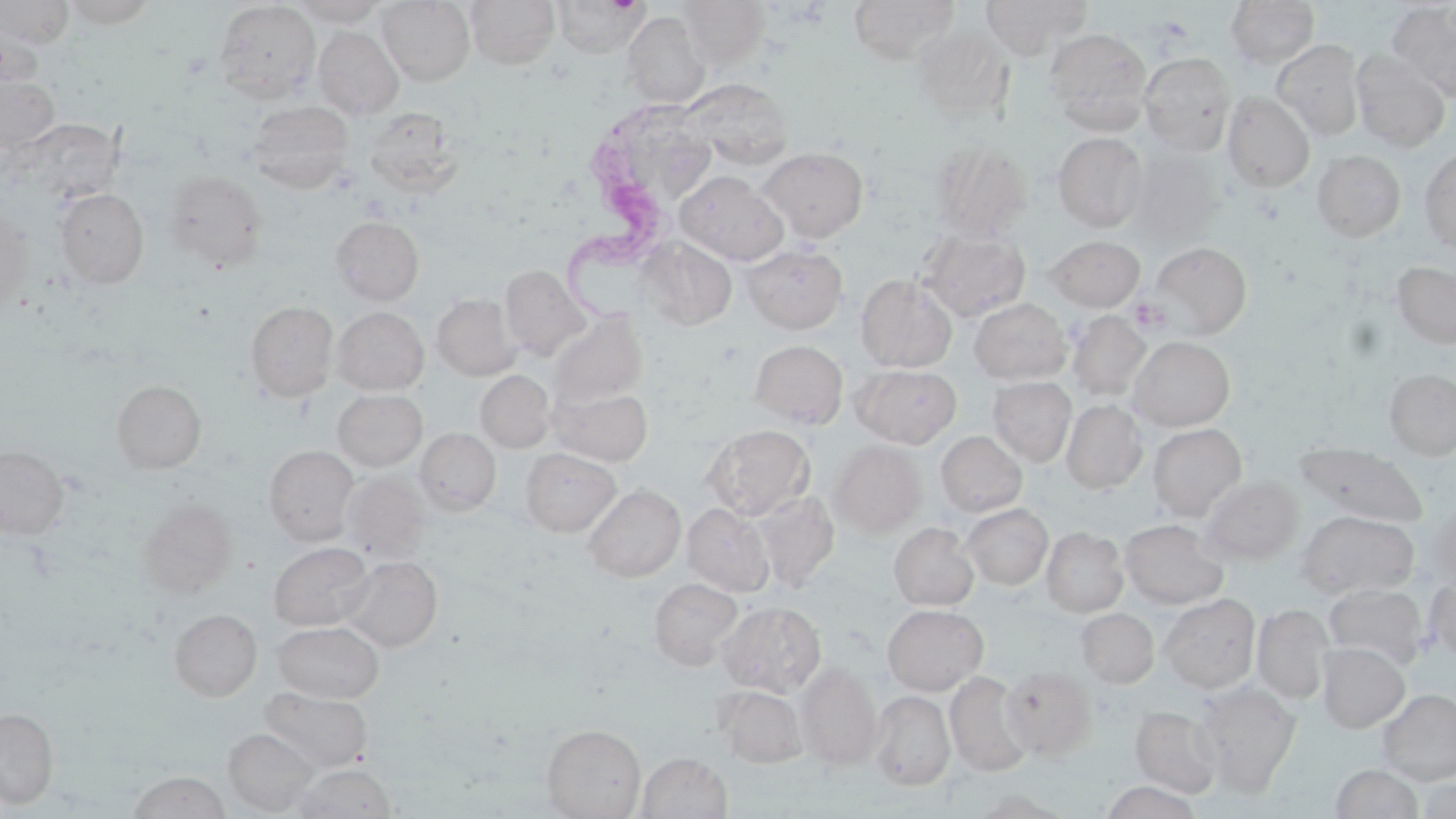
Approximate bounding boxes as [x1, y1, x2, y2] in pixels. Trypanosoma brucei locations: [567, 107, 682, 325]. Uninfected red blood cell locations: [59, 0, 161, 28], [290, 0, 391, 27], [377, 0, 475, 86], [465, 0, 560, 70], [553, 0, 649, 59], [849, 0, 960, 65], [979, 0, 1092, 59], [1225, 0, 1320, 69], [0, 1, 74, 47], [677, 1, 770, 68], [213, 2, 320, 102], [1387, 2, 1456, 102], [622, 11, 710, 109], [0, 19, 45, 94], [911, 24, 1015, 125], [313, 26, 404, 120], [1044, 27, 1153, 135], [1271, 39, 1365, 141], [1350, 50, 1451, 152], [1139, 52, 1237, 155], [0, 75, 61, 156], [681, 78, 793, 169], [1222, 92, 1315, 192], [246, 100, 354, 193], [364, 106, 461, 195], [642, 112, 713, 208], [5, 118, 127, 214], [1053, 132, 1148, 231], [929, 141, 1033, 241], [757, 147, 869, 243], [1126, 147, 1224, 244], [1419, 148, 1456, 254], [1312, 150, 1406, 242], [162, 170, 267, 272], [675, 170, 787, 265], [54, 188, 149, 289], [0, 206, 35, 315], [330, 215, 424, 305], [918, 229, 1030, 321], [1045, 235, 1145, 311], [637, 237, 737, 330], [1149, 241, 1252, 338], [743, 243, 848, 333], [1391, 260, 1456, 349], [499, 264, 590, 360], [855, 274, 958, 372], [432, 292, 520, 380], [969, 298, 1071, 384], [244, 300, 339, 402], [332, 307, 429, 395], [548, 310, 648, 409], [1067, 311, 1151, 402], [1128, 336, 1235, 430], [750, 340, 848, 428], [855, 364, 962, 447], [1384, 368, 1456, 459], [476, 370, 555, 453], [988, 377, 1076, 466], [111, 380, 207, 474], [551, 386, 653, 467], [332, 389, 428, 472], [1062, 400, 1147, 494], [1147, 423, 1246, 520], [703, 425, 815, 520], [415, 428, 501, 516], [936, 430, 1027, 516], [829, 440, 927, 537], [1294, 443, 1428, 527], [0, 444, 68, 540], [263, 445, 359, 544], [521, 447, 621, 535], [340, 472, 430, 560], [1201, 475, 1303, 564], [583, 484, 686, 582], [750, 492, 840, 590], [137, 498, 236, 598], [683, 502, 774, 596], [961, 503, 1053, 590], [1298, 510, 1419, 598], [1119, 519, 1227, 608], [889, 522, 979, 610], [1042, 527, 1128, 617], [268, 541, 375, 631], [339, 556, 442, 652], [1424, 576, 1456, 662], [649, 577, 743, 670], [1323, 583, 1429, 669], [1159, 593, 1260, 692], [718, 601, 826, 697], [882, 604, 988, 694], [1253, 604, 1333, 704], [169, 608, 262, 701], [1077, 608, 1159, 687], [272, 620, 383, 703], [1317, 643, 1409, 732], [796, 662, 882, 770], [1000, 664, 1098, 760], [945, 671, 1034, 777], [1194, 682, 1301, 795], [714, 685, 806, 767], [259, 686, 373, 773], [1378, 689, 1456, 784], [869, 690, 955, 791], [1131, 705, 1222, 796], [0, 708, 59, 808], [541, 724, 645, 819], [223, 728, 319, 815], [636, 751, 733, 818], [291, 763, 398, 818], [1329, 764, 1425, 819], [128, 771, 231, 819], [1415, 775, 1456, 818], [1100, 781, 1204, 819], [967, 788, 1074, 818]. Slide-level diagnosis: Trypanosoma brucei. Single field of view. Image is 1456×819 pixels. May-Grünwald-Giemsa-stained preparation. Captured at 1000x magnification. Light microscopy. Thin blood film.